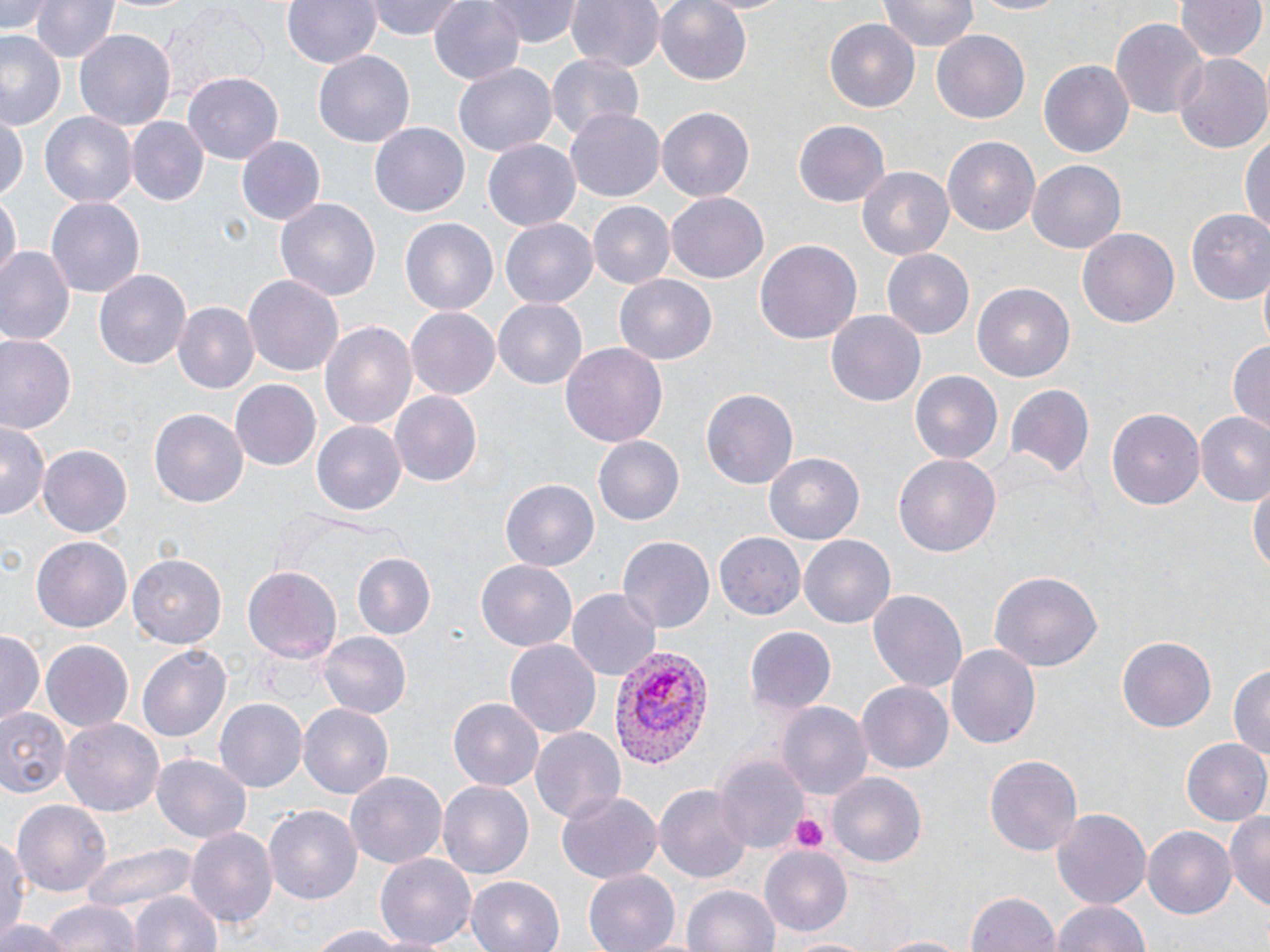
Summary:
  - Coordinate format: approximate bounding boxes as (x1,y1)-(x2,y2) corner pairs in pixels
  - Uninfected red blood cell locations: (3,0)-(61,38), (34,0)-(118,63), (284,0)-(380,69), (366,0)-(467,40), (429,0)-(528,87), (490,0)-(581,47), (565,0)-(663,75), (654,0)-(755,86), (966,0)-(1074,17), (99,1)-(205,19), (878,1)-(980,52), (1177,1)-(1265,63), (1111,17)-(1206,119), (823,19)-(919,113), (74,29)-(177,131), (0,30)-(66,130), (932,32)-(1029,122), (1174,51)-(1270,154), (314,52)-(414,146), (546,53)-(645,142), (1039,60)-(1133,159), (453,65)-(556,156), (185,73)-(282,166), (565,107)-(662,202), (657,107)-(753,202), (40,111)-(136,207), (0,116)-(25,202), (127,118)-(208,205), (793,121)-(889,207), (369,123)-(469,218), (1240,128)-(1269,243), (233,135)-(325,228), (943,136)-(1039,237), (483,139)-(581,231), (1028,161)-(1126,253), (859,166)-(956,261), (1,191)-(18,283), (667,194)-(768,282), (44,195)-(148,298), (276,198)-(379,305), (587,201)-(673,289), (1184,210)-(1270,305), (400,218)-(498,317), (500,219)-(597,309), (1078,227)-(1180,330), (755,238)-(861,346), (0,248)-(74,346), (881,250)-(974,340), (93,269)-(191,370), (1258,272)-(1269,358), (243,273)-(343,379), (611,273)-(716,366), (972,283)-(1074,383), (494,297)-(592,388), (173,302)-(258,394), (407,307)-(498,399), (827,312)-(925,406), (321,320)-(417,434), (2,336)-(76,435), (1228,339)-(1270,431), (559,343)-(667,450), (910,371)-(1003,467), (229,379)-(322,472), (1003,381)-(1096,478), (701,387)-(798,489), (390,392)-(482,488), (1107,407)-(1203,512), (149,409)-(247,508), (1196,411)-(1270,506), (0,422)-(48,522), (311,422)-(404,517), (594,437)-(685,526), (38,441)-(132,536), (766,452)-(865,545), (893,453)-(1001,560), (1249,475)-(1269,584), (500,478)-(598,569), (714,530)-(807,619), (800,535)-(895,630), (619,536)-(715,631), (32,538)-(131,631), (129,551)-(227,649), (351,553)-(435,641), (476,560)-(578,651), (244,566)-(341,666), (988,570)-(1104,672), (567,588)-(658,681), (867,588)-(968,695), (745,626)-(836,718), (319,631)-(410,720), (1,632)-(43,725), (1118,634)-(1216,730), (41,639)-(134,731), (504,639)-(600,738), (946,642)-(1040,751), (137,643)-(231,743), (1230,660)-(1270,763), (856,681)-(955,773), (214,696)-(307,790), (449,699)-(542,791), (776,700)-(874,801), (297,703)-(394,801), (3,710)-(70,796), (61,716)-(165,816), (529,725)-(627,825), (1181,739)-(1270,828), (154,754)-(253,844), (985,754)-(1081,855), (714,755)-(809,855), (346,770)-(450,869), (830,774)-(925,869), (437,781)-(533,879), (656,782)-(752,886), (555,792)-(660,885), (12,798)-(115,897), (264,805)-(362,905), (1052,809)-(1151,907), (1226,809)-(1270,913), (1142,825)-(1233,915), (184,828)-(277,931), (1,832)-(25,951), (80,843)-(198,916), (759,846)-(852,937), (375,854)-(474,950), (583,870)-(680,952), (467,875)-(563,952), (682,883)-(780,952), (964,890)-(1061,952), (127,891)-(223,952), (42,898)-(140,952), (1050,898)-(1150,952), (3,914)-(70,952), (301,922)-(428,951), (781,933)-(873,952), (870,933)-(971,952)
  - Platelet locations: (788,811)-(829,853)
  - Plasmodium vivax-infected red blood cell locations: (612,642)-(717,769)
  - Slide-level diagnosis: Plasmodium vivax
  - Stain: May-Grünwald-Giemsa
  - Field of view: one of a larger specimen
  - Magnification: 1000x
  - Preparation: thin blood smear
  - Image size: 1270×952 pixels
  - Modality: light microscopy